State which parasite is depicted.
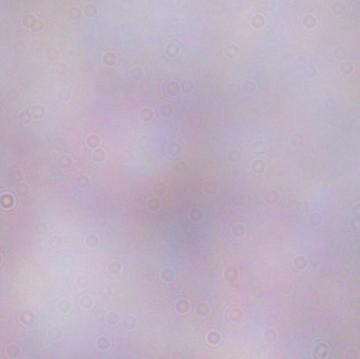
A trypanosome.

modality = photomicrograph
magnification = 1000x